Describe the morphology of the erythrocytes.
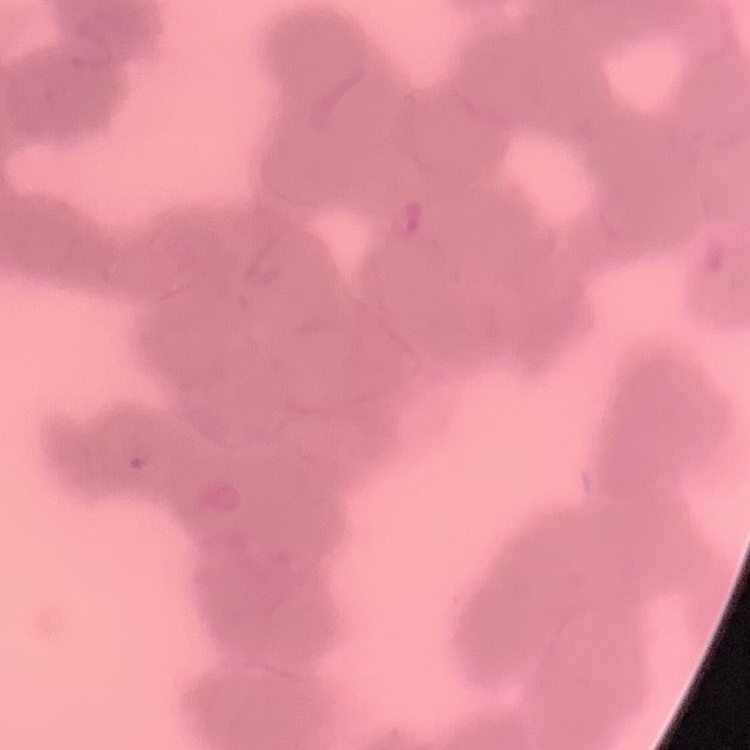
They show rouleaux formation.

Summary:
  - Stain: Field's or Giemsa
  - Preparation: thin blood smear
  - Image type: square crop of a larger photomicrograph